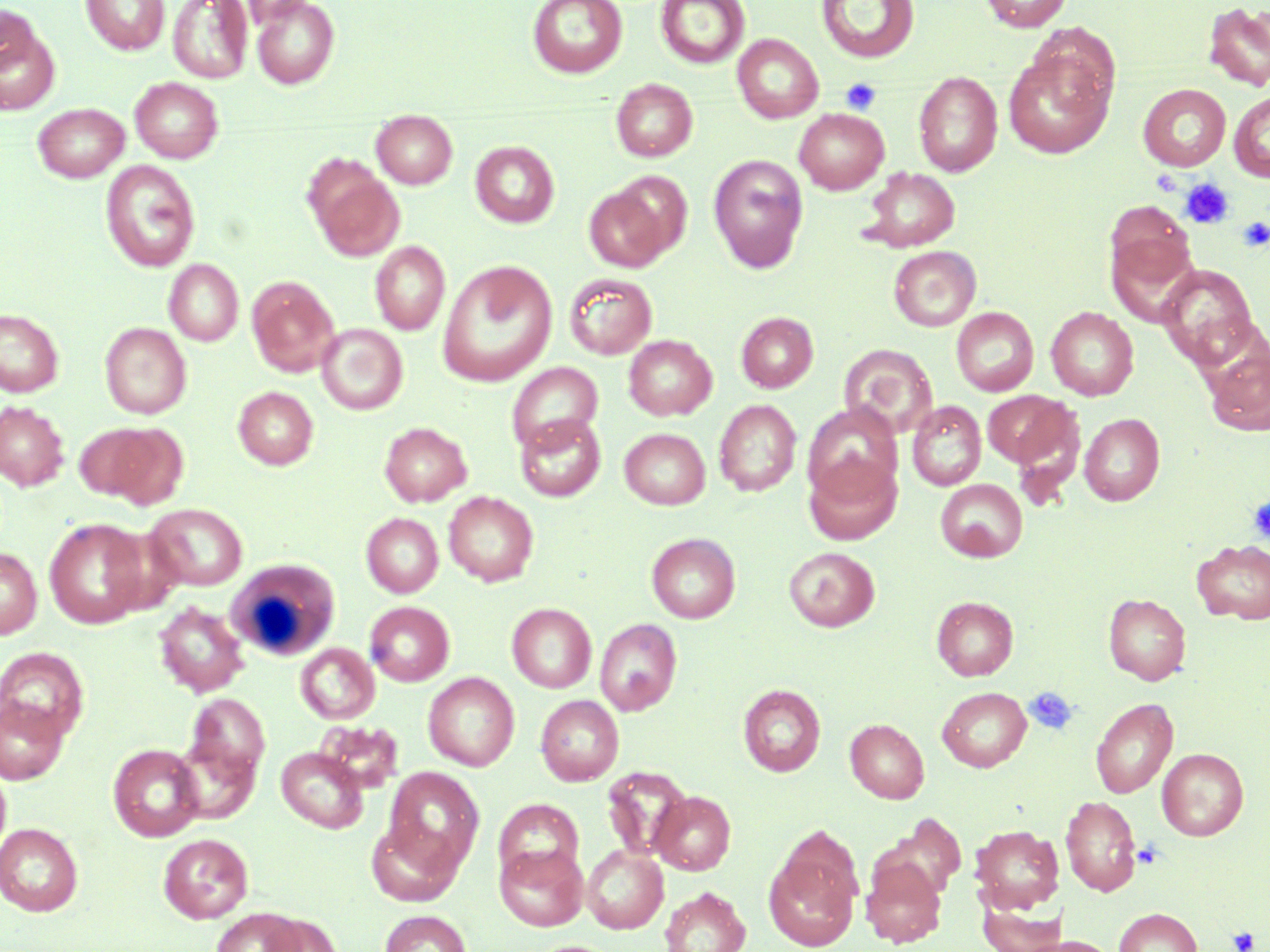 Approximate bounding boxes as (x1, y1, x2, y2) in pixels. Uninfected red blood cell locations: (81, 0, 170, 55), (168, 0, 253, 83), (250, 0, 340, 89), (527, 0, 628, 78), (655, 0, 750, 69), (816, 0, 920, 63), (980, 0, 1072, 32), (1203, 2, 1270, 92), (0, 4, 41, 78), (0, 20, 60, 115), (732, 34, 824, 123), (1002, 46, 1116, 159), (913, 71, 1002, 177), (130, 77, 223, 163), (611, 78, 698, 162), (1138, 84, 1231, 171), (1229, 90, 1270, 182), (33, 102, 130, 182), (794, 108, 889, 194), (372, 110, 458, 189), (470, 140, 560, 228), (708, 154, 808, 273), (100, 160, 200, 273), (308, 164, 405, 262), (860, 167, 960, 252), (583, 184, 676, 273), (1103, 201, 1200, 308), (370, 241, 450, 335), (888, 245, 981, 331), (164, 259, 243, 346), (437, 260, 557, 386), (1157, 263, 1259, 370), (564, 272, 657, 359), (247, 276, 339, 376), (1046, 306, 1139, 401), (951, 307, 1038, 396), (0, 309, 64, 397), (736, 312, 818, 393), (100, 322, 192, 418), (316, 323, 408, 414), (624, 334, 716, 420), (1204, 340, 1270, 437), (839, 343, 938, 440), (506, 362, 603, 454), (233, 386, 318, 470), (982, 389, 1079, 472), (714, 399, 801, 496), (907, 400, 986, 491), (0, 401, 69, 491), (802, 402, 903, 500), (1079, 413, 1165, 506), (515, 414, 606, 501), (74, 422, 165, 503), (379, 422, 472, 506), (619, 428, 711, 509), (803, 453, 902, 545), (935, 478, 1027, 562), (443, 491, 538, 586), (145, 503, 248, 590), (361, 512, 443, 597), (44, 517, 150, 628), (646, 532, 741, 623), (1192, 539, 1270, 625), (784, 546, 880, 632), (0, 547, 42, 640), (1104, 593, 1191, 685), (932, 596, 1018, 681), (153, 601, 249, 697), (365, 601, 454, 686), (506, 602, 597, 692), (595, 618, 682, 716), (296, 643, 380, 723), (0, 646, 89, 742), (423, 672, 519, 771), (738, 684, 826, 776), (937, 686, 1031, 772), (184, 692, 270, 785), (0, 695, 69, 785), (536, 695, 624, 786), (1091, 697, 1178, 798), (845, 718, 929, 803), (314, 719, 404, 794), (172, 734, 261, 824), (108, 743, 204, 842), (277, 747, 368, 833), (1157, 748, 1248, 840), (0, 763, 11, 861), (384, 767, 484, 872), (602, 767, 692, 861), (650, 791, 735, 874), (1060, 795, 1141, 896), (495, 798, 584, 884), (366, 818, 464, 907), (0, 823, 84, 916), (970, 824, 1064, 912), (158, 833, 254, 923), (496, 844, 587, 931), (581, 845, 669, 933), (764, 845, 861, 951), (861, 857, 947, 948), (660, 887, 750, 952), (977, 894, 1065, 952), (211, 907, 305, 952), (1114, 907, 1202, 952), (379, 910, 472, 952), (262, 914, 342, 952), (1023, 936, 1119, 952), (527, 940, 623, 952). Platelet locations: (841, 78, 881, 114), (1180, 178, 1235, 229), (1237, 217, 1270, 251), (1248, 498, 1270, 542), (1024, 687, 1079, 735), (1133, 840, 1164, 868), (1227, 927, 1258, 952). White blood cell locations: (227, 559, 340, 661). Slide-level diagnosis: negative for blood parasites. Light microscopy. One field of a larger specimen. May-Grünwald-Giemsa stain. 1000x magnification. Image is 1270×952 pixels. Thin blood film.